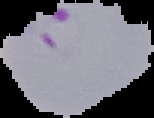
Summary:
  - Preparation: thin blood film
  - Image size: 154×118 pixels
  - Malaria status: parasitized
  - Image type: segmented cell region on a black background